Assess this cell for malaria.
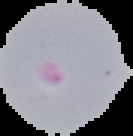
It is parasitized.

Image is 133×136 pixels. Segmented cell region on a black background. From a thin blood smear.